Locate every Plasmodium parasite.
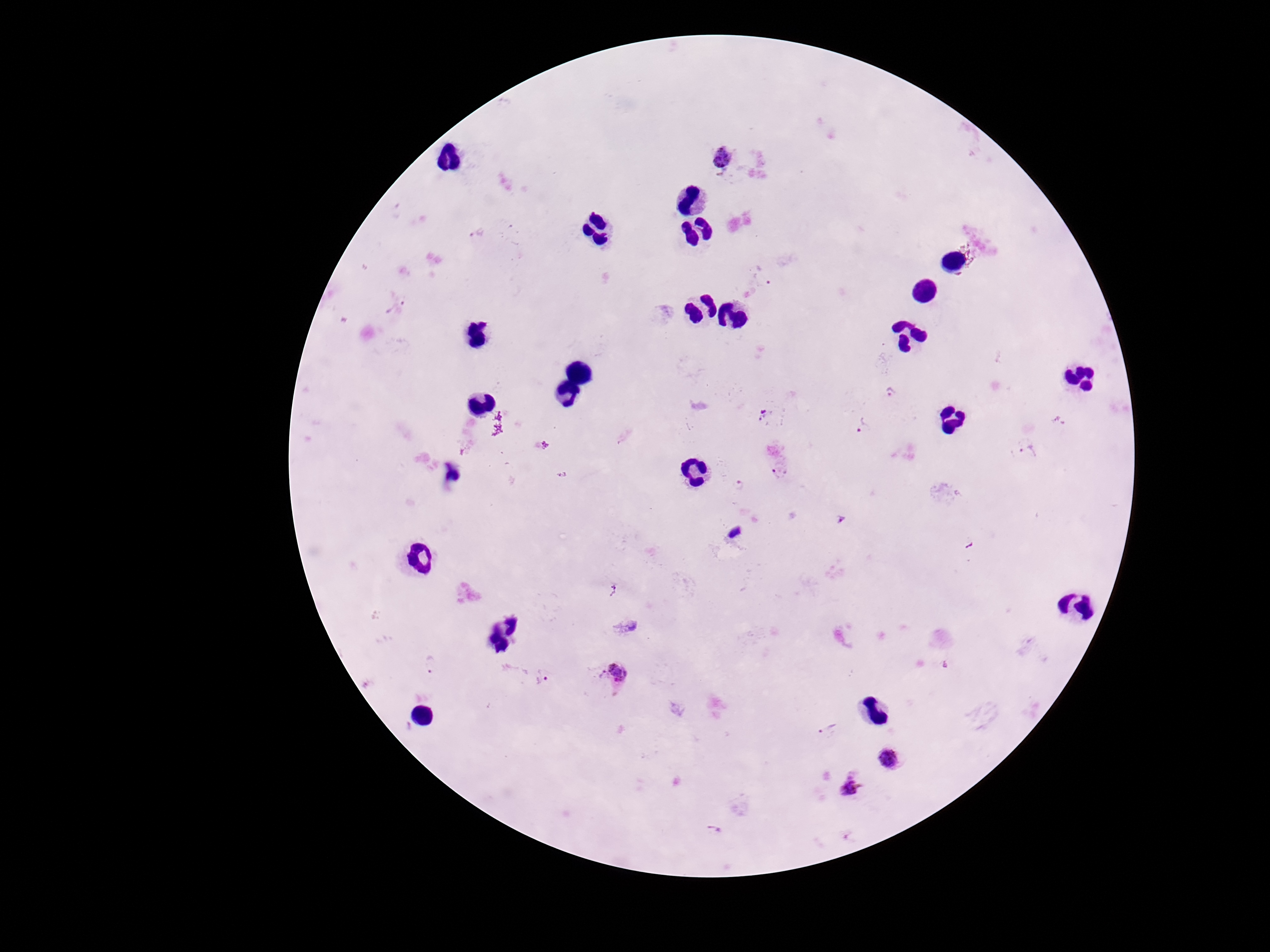
Approximate centers as [x, y] in pixels.
Plasmodium parasites: [724, 158], [476, 234], [761, 280], [396, 304], [890, 393], [763, 415], [862, 426], [1029, 452], [779, 470], [739, 485], [430, 664], [618, 675], [543, 678], [829, 729], [888, 760], [850, 789], [714, 830].

image size = 1270×952 pixels
stain = Giemsa
capture = smartphone camera through the microscope eyepiece
magnification = 100x
patient malaria status = infected
field of view = single
preparation = thick blood film